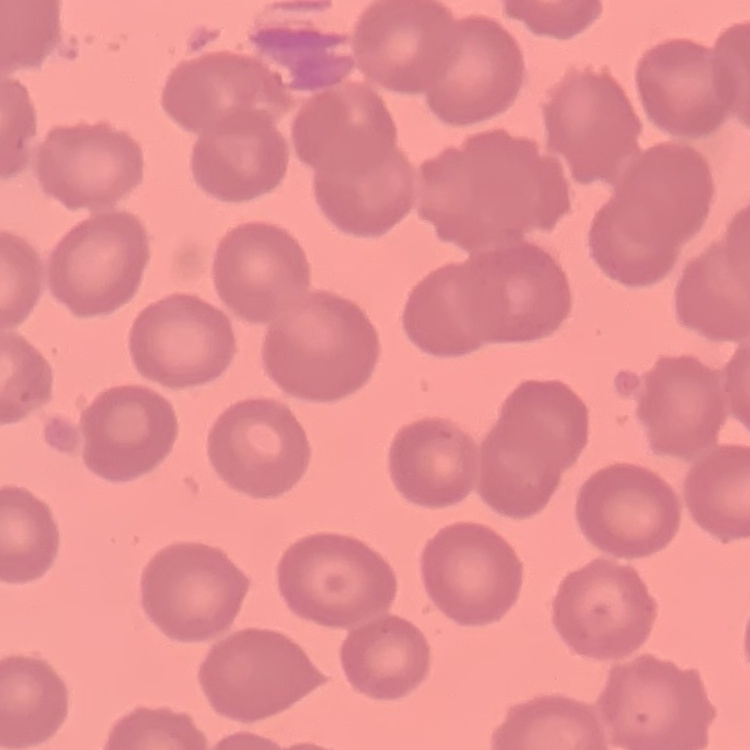

Summary:
  - Red blood cell morphology: no rouleaux formation
  - Stain: Field's or Giemsa
  - Image type: one tile cut from a larger photomicrograph
  - Preparation: thin blood film